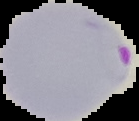
image size = 139×121 pixels
preparation = thin blood film
malaria status = parasitized
image type = cell region segmented out of the field of view; surrounding area masked to black